Name the parasite shown.
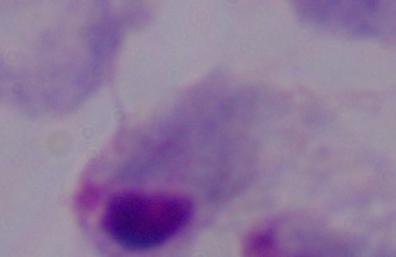

A trichomonad.

1000x magnification. Photomicrograph.